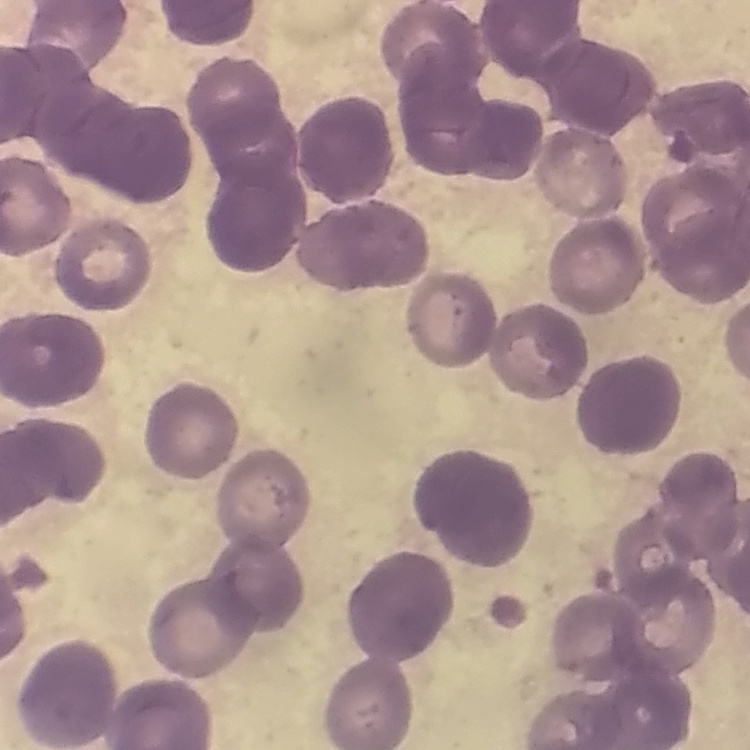
The erythrocytes exhibit rouleaux formation. One tile cut from a larger photomicrograph. Stained with either Field's or Giemsa. Thin blood smear.